Report the malaria status of this cell.
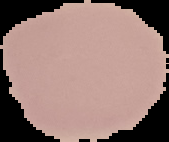
It is uninfected.

Cell region segmented out of the field of view; the surrounding area is masked to black. Image is 169×142 pixels. From a thin blood smear.